Assess this cell for malaria.
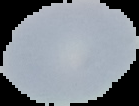

It is uninfected.

Segmented cell region on a black background. Image is 139×106 pixels. From a thin blood film.